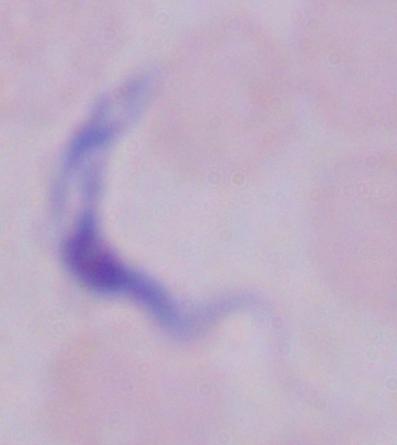

1000x magnification. A trypanosome is shown. Micrograph.